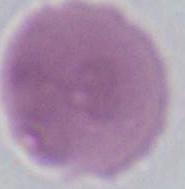

Micrograph. 1000x magnification. A red blood cell is shown.